Locate every blood parasite and identify its species.
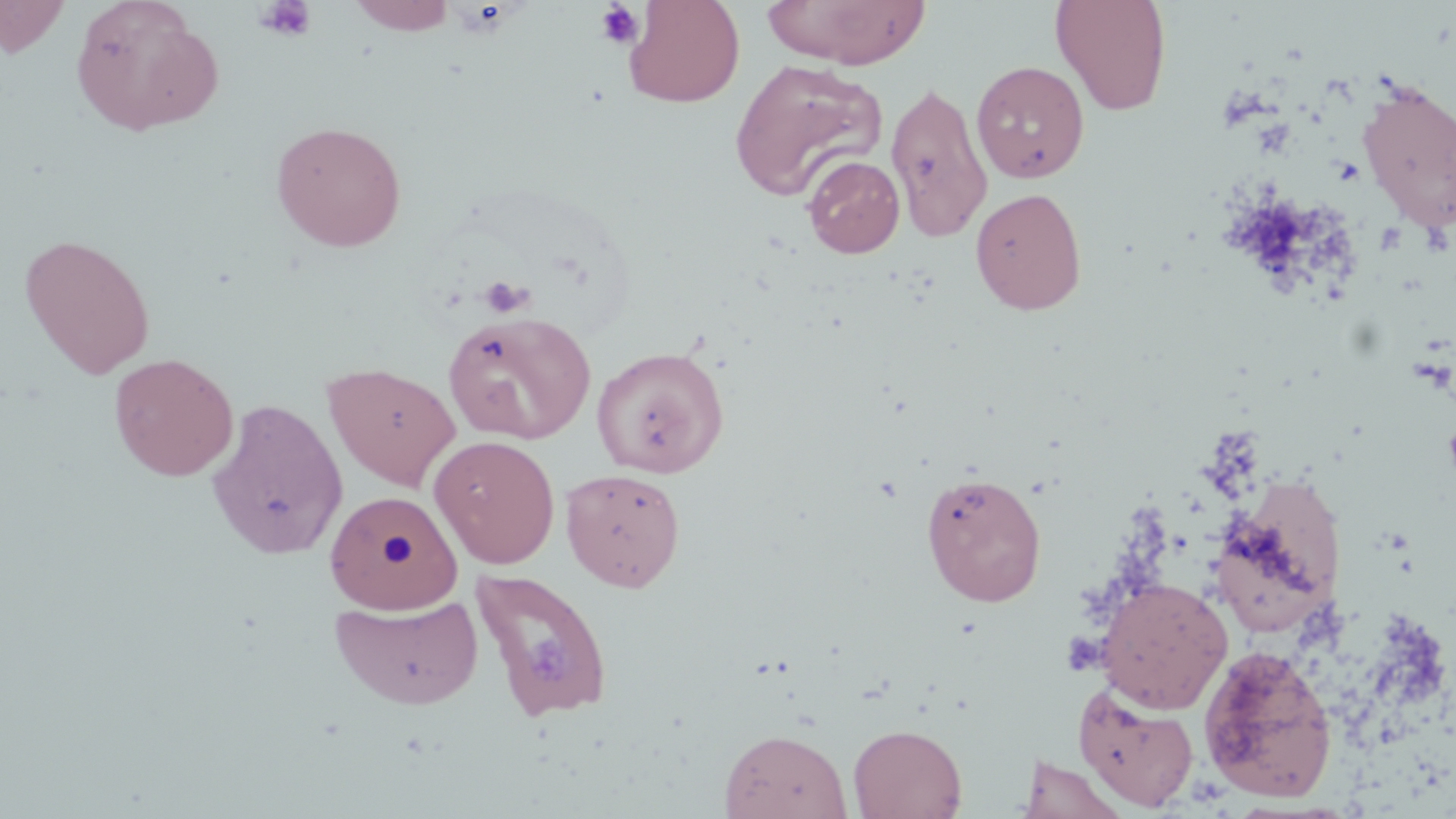
No blood parasites observed.

{
  "slide_level_diagnosis": "no evidence of blood parasites",
  "modality": "optical microscopy",
  "preparation": "thin blood smear",
  "uninfected_red_blood_cell_locations": "approximate bounding boxes as (x1, y1, x2, y2) in pixels: (0, 0, 72, 57), (349, 0, 457, 35), (761, 0, 931, 69), (1051, 0, 1172, 117), (70, 1, 224, 137), (623, 1, 744, 107), (728, 59, 888, 204), (971, 60, 1090, 183), (1357, 80, 1456, 234), (886, 81, 993, 243), (271, 120, 407, 252), (802, 155, 905, 258), (970, 187, 1087, 315), (20, 233, 156, 379), (443, 311, 596, 445), (592, 345, 729, 479), (109, 353, 239, 482), (324, 362, 461, 492), (207, 398, 347, 560), (429, 435, 560, 568), (561, 467, 686, 592), (920, 471, 1047, 607), (1209, 484, 1344, 639), (324, 490, 463, 615), (470, 568, 615, 724), (1096, 577, 1233, 714), (329, 592, 484, 710), (1198, 644, 1338, 803), (1074, 682, 1200, 812), (848, 723, 967, 819), (719, 728, 853, 818), (1018, 754, 1129, 819)",
  "platelet_locations": "approximate bounding boxes as (x1, y1, x2, y2) in pixels: (254, 0, 317, 42), (594, 2, 645, 50), (479, 276, 532, 318)",
  "stain": "May-Grünwald-Giemsa",
  "magnification": "1000x",
  "field_of_view": "one of a larger specimen",
  "image_size": "1456×819 pixels"
}